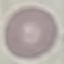

{
  "malaria_status": "uninfected",
  "preparation": "thin blood smear",
  "capture": "smartphone through the microscope eyepiece",
  "image_type": "automatically extracted cell patch, resized to 64 × 64 pixels",
  "stain": "Giemsa"
}